State which cell type is depicted.
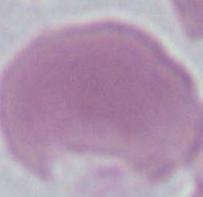
An erythrocyte.

Summary:
  - Magnification: 1000x
  - Modality: micrograph